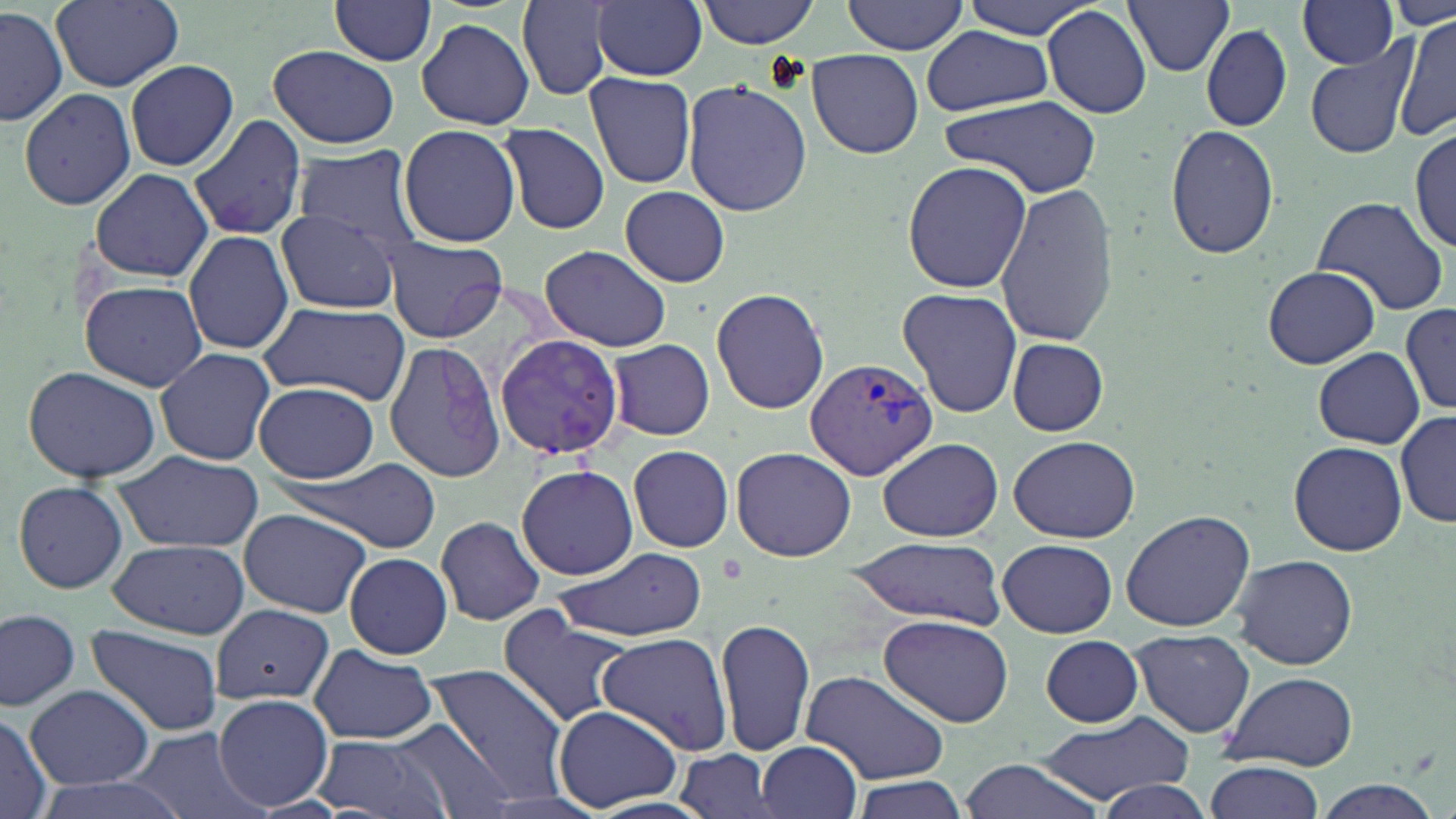
Approximate bounding boxes as named x1/y1/x2/y2 corners in pixels. Uninfected red blood cell locations: (x1=50, y1=0, x2=184, y2=90), (x1=697, y1=0, x2=821, y2=48), (x1=843, y1=0, x2=969, y2=55), (x1=962, y1=0, x2=1107, y2=37), (x1=1123, y1=0, x2=1236, y2=76), (x1=1387, y1=0, x2=1455, y2=31), (x1=331, y1=1, x2=437, y2=67), (x1=593, y1=1, x2=708, y2=80), (x1=518, y1=2, x2=613, y2=101), (x1=1299, y1=2, x2=1399, y2=69), (x1=1042, y1=6, x2=1153, y2=119), (x1=0, y1=7, x2=67, y2=129), (x1=1395, y1=15, x2=1456, y2=141), (x1=416, y1=17, x2=536, y2=129), (x1=1202, y1=24, x2=1293, y2=130), (x1=921, y1=25, x2=1054, y2=116), (x1=1303, y1=38, x2=1419, y2=159), (x1=267, y1=45, x2=400, y2=150), (x1=808, y1=50, x2=923, y2=158), (x1=124, y1=60, x2=239, y2=172), (x1=584, y1=69, x2=698, y2=190), (x1=683, y1=76, x2=811, y2=217), (x1=19, y1=88, x2=137, y2=211), (x1=939, y1=94, x2=1103, y2=198), (x1=187, y1=113, x2=307, y2=242), (x1=498, y1=122, x2=610, y2=235), (x1=1165, y1=123, x2=1280, y2=259), (x1=398, y1=124, x2=521, y2=247), (x1=1411, y1=124, x2=1455, y2=254), (x1=294, y1=147, x2=424, y2=248), (x1=902, y1=161, x2=1032, y2=292), (x1=89, y1=168, x2=214, y2=282), (x1=994, y1=182, x2=1120, y2=345), (x1=620, y1=185, x2=731, y2=287), (x1=1312, y1=195, x2=1452, y2=319), (x1=272, y1=210, x2=403, y2=314), (x1=186, y1=230, x2=295, y2=357), (x1=382, y1=235, x2=508, y2=343), (x1=539, y1=246, x2=670, y2=351), (x1=1262, y1=265, x2=1384, y2=370), (x1=77, y1=279, x2=209, y2=391), (x1=711, y1=287, x2=831, y2=414), (x1=896, y1=287, x2=1023, y2=418), (x1=258, y1=301, x2=410, y2=403), (x1=1399, y1=304, x2=1456, y2=414), (x1=498, y1=332, x2=620, y2=461), (x1=1006, y1=337, x2=1108, y2=437), (x1=381, y1=339, x2=507, y2=483), (x1=608, y1=340, x2=716, y2=441), (x1=153, y1=347, x2=276, y2=465), (x1=1314, y1=348, x2=1424, y2=448), (x1=22, y1=364, x2=162, y2=485), (x1=255, y1=381, x2=378, y2=483), (x1=1396, y1=411, x2=1455, y2=528), (x1=1008, y1=434, x2=1140, y2=543), (x1=879, y1=437, x2=1002, y2=543), (x1=1289, y1=440, x2=1407, y2=556), (x1=627, y1=443, x2=736, y2=553), (x1=732, y1=447, x2=855, y2=563), (x1=115, y1=451, x2=264, y2=556), (x1=285, y1=456, x2=446, y2=554), (x1=516, y1=463, x2=638, y2=581), (x1=11, y1=481, x2=130, y2=592), (x1=237, y1=508, x2=371, y2=618), (x1=1121, y1=509, x2=1256, y2=633), (x1=435, y1=514, x2=546, y2=626), (x1=846, y1=537, x2=1008, y2=628), (x1=998, y1=538, x2=1116, y2=639), (x1=103, y1=539, x2=248, y2=637), (x1=555, y1=546, x2=708, y2=642), (x1=345, y1=551, x2=452, y2=659), (x1=1229, y1=553, x2=1361, y2=672), (x1=210, y1=604, x2=333, y2=703), (x1=495, y1=607, x2=633, y2=727), (x1=0, y1=609, x2=81, y2=711), (x1=879, y1=614, x2=1016, y2=730), (x1=716, y1=615, x2=816, y2=760), (x1=85, y1=624, x2=226, y2=740), (x1=811, y1=624, x2=991, y2=760), (x1=1130, y1=629, x2=1254, y2=738), (x1=597, y1=632, x2=735, y2=757), (x1=1041, y1=636, x2=1142, y2=727), (x1=307, y1=645, x2=438, y2=746), (x1=426, y1=662, x2=571, y2=801), (x1=802, y1=669, x2=952, y2=785), (x1=1220, y1=670, x2=1359, y2=772), (x1=27, y1=686, x2=154, y2=788), (x1=214, y1=694, x2=334, y2=812), (x1=554, y1=705, x2=683, y2=812), (x1=0, y1=709, x2=51, y2=819), (x1=1034, y1=710, x2=1193, y2=803), (x1=387, y1=717, x2=519, y2=819), (x1=130, y1=728, x2=262, y2=819), (x1=310, y1=734, x2=454, y2=819), (x1=755, y1=738, x2=862, y2=819), (x1=678, y1=749, x2=779, y2=819), (x1=955, y1=759, x2=1105, y2=819), (x1=1204, y1=760, x2=1325, y2=817), (x1=24, y1=773, x2=197, y2=819), (x1=849, y1=776, x2=970, y2=819), (x1=1088, y1=779, x2=1219, y2=819), (x1=1307, y1=781, x2=1444, y2=819). Plasmodium vivax-infected red blood cell locations: (x1=805, y1=357, x2=938, y2=481). Slide-level diagnosis: Plasmodium vivax. Captured at 1000x magnification. Optical microscopy. One field of a larger specimen. May-Grünwald-Giemsa stain. Thin blood film. Image is 1456×819 pixels.